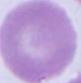
A red blood cell is shown. Micrograph. 1000x magnification.